State the blood parasite species.
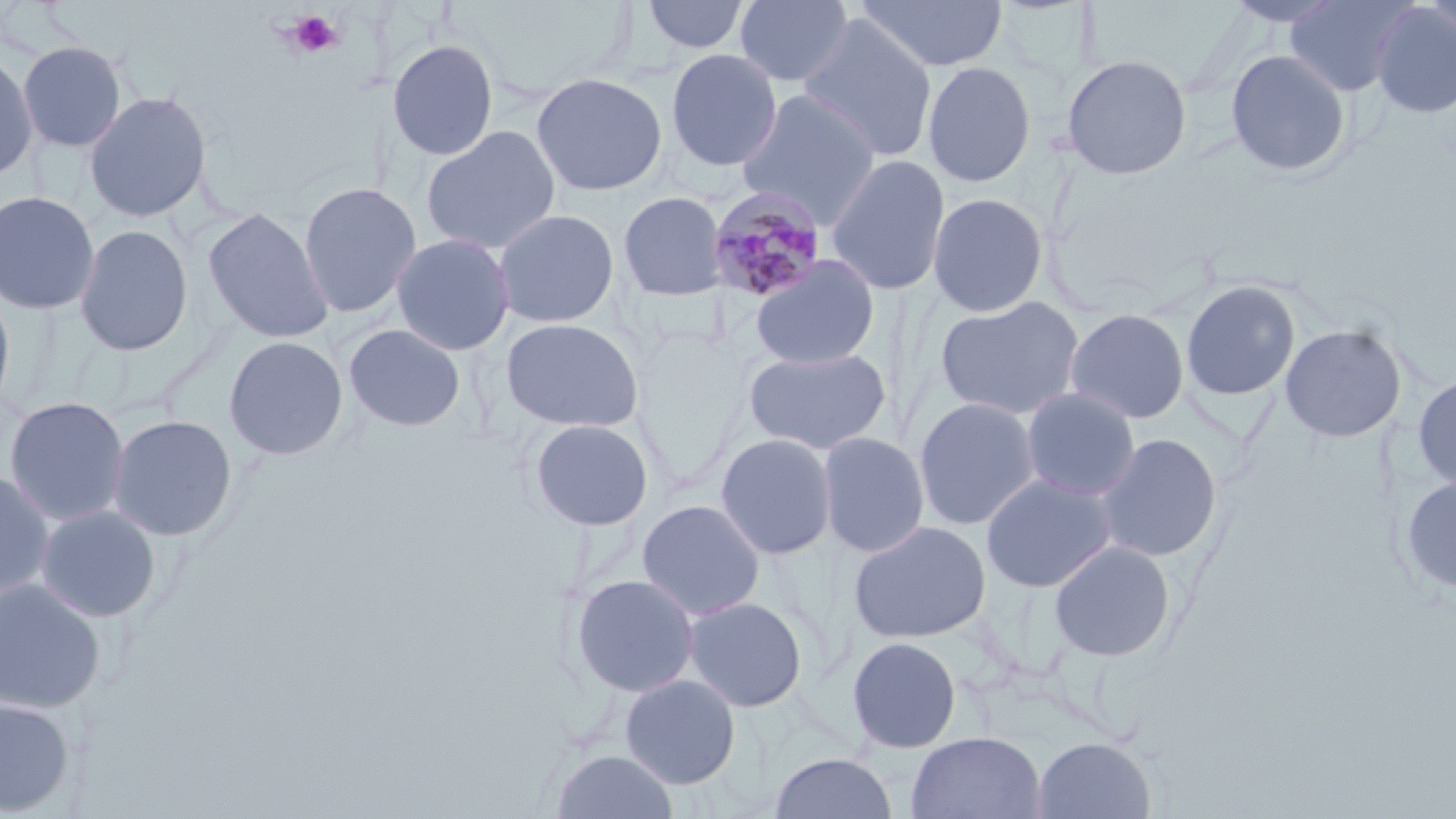

Plasmodium malariae.

Approximate bounding boxes as (x1, y1, x2, y2) in pixels. Plasmodium malariae-infected red blood cell locations: (707, 187, 828, 304). Uninfected red blood cell locations: (641, 0, 751, 56), (733, 0, 855, 88), (855, 0, 1007, 73), (1223, 0, 1345, 28), (1283, 0, 1417, 96), (1418, 0, 1456, 44), (1370, 3, 1456, 119), (797, 14, 939, 163), (386, 38, 499, 161), (18, 40, 128, 152), (1225, 48, 1351, 178), (0, 49, 39, 183), (665, 49, 782, 171), (1060, 53, 1193, 179), (922, 61, 1037, 188), (531, 72, 668, 196), (84, 90, 212, 223), (736, 90, 881, 225), (421, 124, 562, 255), (826, 154, 950, 296), (298, 181, 421, 318), (0, 190, 100, 315), (618, 191, 728, 301), (927, 191, 1049, 317), (202, 206, 335, 344), (493, 208, 620, 328), (74, 223, 193, 357), (391, 232, 515, 356), (750, 255, 880, 371), (1180, 280, 1301, 401), (0, 283, 17, 422), (934, 295, 1085, 420), (1064, 308, 1190, 424), (501, 317, 644, 432), (343, 323, 467, 432), (1280, 323, 1407, 443), (223, 335, 348, 460), (742, 346, 892, 455), (1412, 372, 1456, 494), (1020, 387, 1141, 501), (3, 396, 130, 526), (913, 396, 1041, 530), (107, 414, 238, 541), (528, 418, 655, 532), (817, 431, 930, 557), (715, 433, 837, 560), (1096, 433, 1222, 562), (0, 469, 55, 600), (981, 473, 1116, 592), (1399, 474, 1456, 596), (637, 499, 766, 620), (35, 505, 161, 622), (849, 520, 991, 643), (1049, 540, 1176, 662), (570, 574, 700, 698), (0, 577, 106, 712), (683, 596, 808, 712), (846, 636, 962, 753), (619, 674, 741, 789), (0, 697, 76, 816), (906, 731, 1047, 819), (1032, 736, 1157, 818), (549, 750, 680, 819), (769, 752, 897, 818). Platelet locations: (286, 9, 342, 58). One field of a larger specimen. Image is 1456×819 pixels. Thin blood film. Captured at 1000x magnification. May-Grünwald-Giemsa-stained preparation. Light microscopy.